Locate and identify every blood parasite.
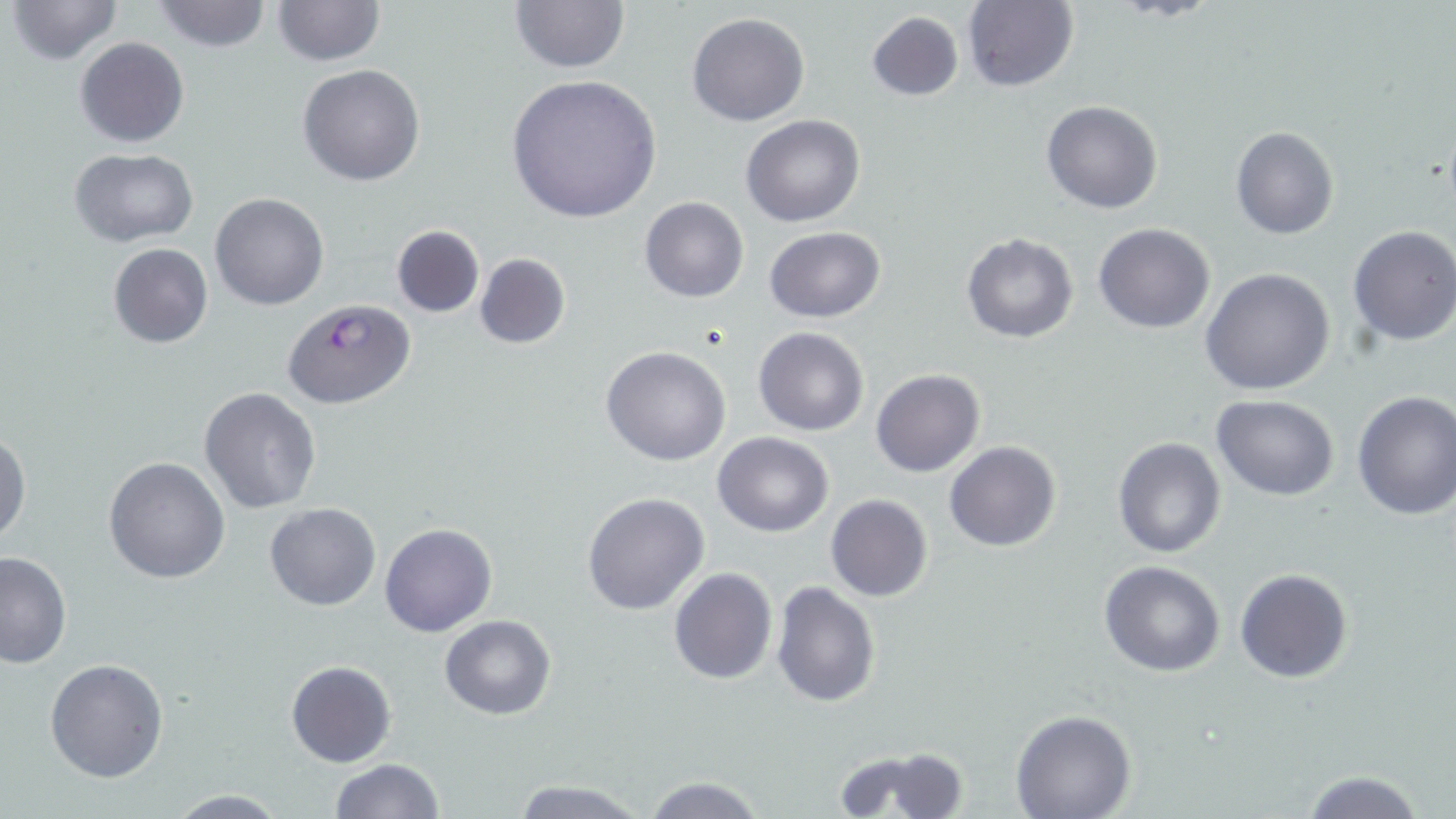

Approximate bounding boxes as (x1,y1)-(x2,y2) corner pairs in pixels.
Plasmodium falciparum-infected red blood cells: (283,299)-(415,409).
No Plasmodium ovale, Plasmodium malariae, Plasmodium vivax, Babesia divergens, or Trypanosoma brucei observed.

{
  "slide_level_diagnosis": "Plasmodium falciparum",
  "preparation": "thin blood smear",
  "magnification": "1000x",
  "uninfected_red_blood_cell_locations": "approximate bounding boxes as (x1,y1)-(x2,y2) corner pairs in pixels: (7,0)-(123,66), (152,0)-(273,53), (271,0)-(384,67), (960,0)-(1079,92), (509,2)-(631,74), (864,10)-(964,102), (687,12)-(811,127), (74,37)-(190,149), (297,64)-(426,186), (504,73)-(663,224), (1042,100)-(1164,215), (740,113)-(866,227), (1231,126)-(1339,240), (68,147)-(199,247), (210,193)-(328,310), (640,196)-(748,303), (1094,223)-(1215,333), (391,225)-(485,318), (1346,225)-(1456,347), (763,226)-(886,323), (961,233)-(1078,343), (107,243)-(214,348), (474,252)-(571,349), (1201,267)-(1334,396), (752,326)-(870,436), (601,345)-(731,465), (870,368)-(987,477), (198,388)-(321,514), (1351,389)-(1456,520), (1211,393)-(1341,502), (0,432)-(29,549), (714,432)-(834,537), (1112,435)-(1226,559), (944,441)-(1061,552), (103,456)-(230,583), (583,491)-(710,615), (826,494)-(933,602), (265,503)-(381,611), (380,523)-(497,638), (0,551)-(72,668), (1099,561)-(1226,677), (668,566)-(777,685), (1234,568)-(1354,684), (771,580)-(880,706), (441,615)-(556,720), (44,657)-(168,781), (286,661)-(396,767), (1011,710)-(1135,819), (834,745)-(970,818), (329,759)-(444,818), (1300,770)-(1427,819), (641,775)-(769,818), (507,777)-(649,818), (162,790)-(292,818)",
  "field_of_view": "single",
  "stain": "May-Grünwald-Giemsa",
  "image_size": "1456×819 pixels",
  "modality": "light microscopy"
}